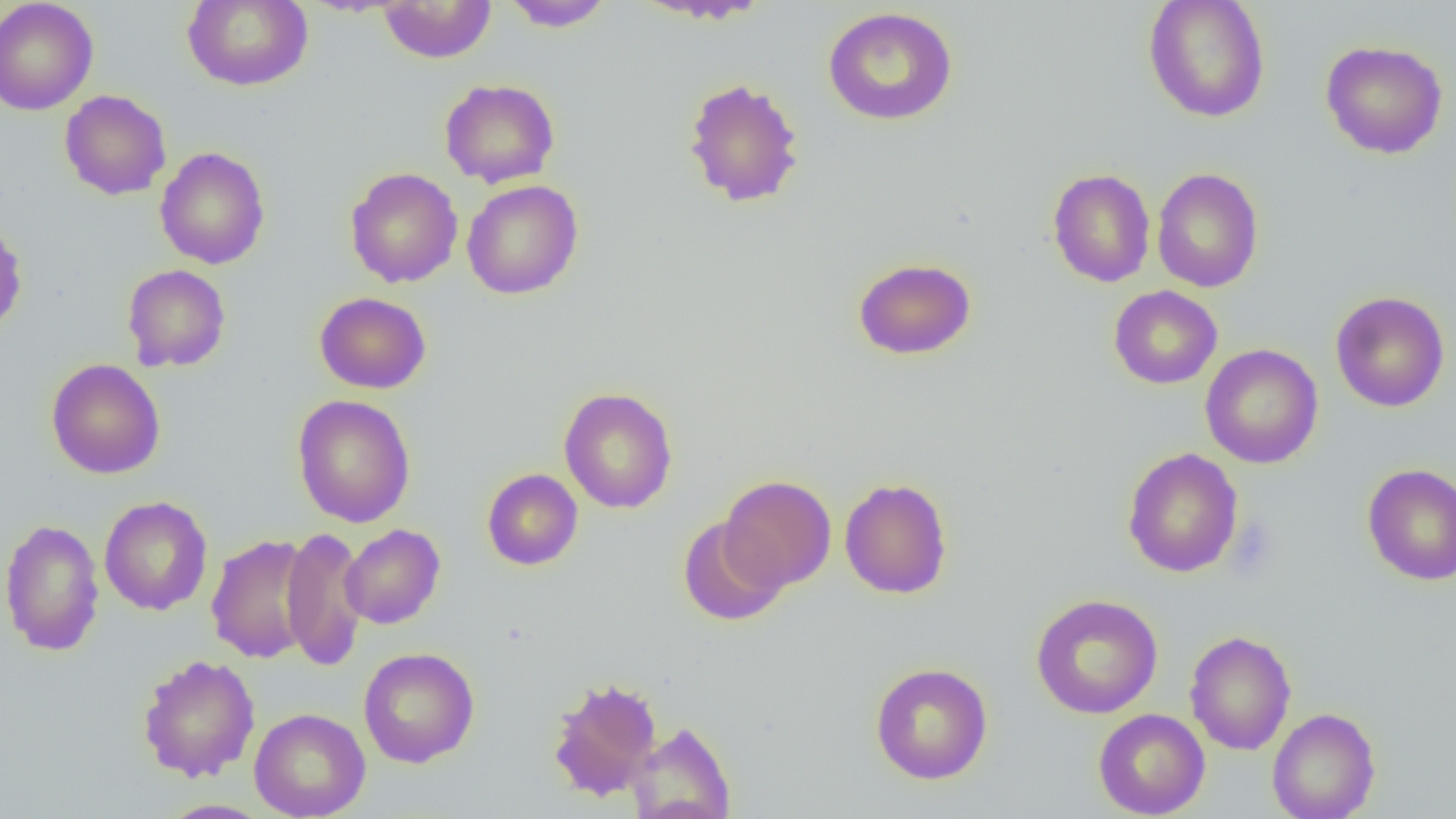 Approximate bounding boxes as named x1/y1/x2/y2 corners in pixels. Uninfected red blood cell locations: (x1=0, y1=0, x2=99, y2=116), (x1=182, y1=0, x2=313, y2=91), (x1=502, y1=0, x2=615, y2=32), (x1=631, y1=0, x2=773, y2=25), (x1=1143, y1=0, x2=1271, y2=123), (x1=377, y1=1, x2=496, y2=63), (x1=822, y1=6, x2=958, y2=126), (x1=1320, y1=40, x2=1448, y2=159), (x1=682, y1=76, x2=805, y2=208), (x1=439, y1=78, x2=560, y2=188), (x1=59, y1=90, x2=172, y2=200), (x1=154, y1=146, x2=270, y2=270), (x1=344, y1=167, x2=463, y2=288), (x1=1151, y1=167, x2=1264, y2=293), (x1=1047, y1=168, x2=1156, y2=287), (x1=462, y1=179, x2=584, y2=300), (x1=0, y1=218, x2=27, y2=337), (x1=852, y1=257, x2=977, y2=360), (x1=121, y1=264, x2=231, y2=372), (x1=1108, y1=285, x2=1223, y2=389), (x1=314, y1=291, x2=431, y2=394), (x1=1331, y1=291, x2=1450, y2=413), (x1=1200, y1=344, x2=1324, y2=469), (x1=46, y1=359, x2=165, y2=479), (x1=558, y1=387, x2=678, y2=513), (x1=292, y1=394, x2=416, y2=528), (x1=1122, y1=447, x2=1243, y2=578), (x1=1362, y1=463, x2=1456, y2=586), (x1=482, y1=468, x2=583, y2=570), (x1=720, y1=475, x2=836, y2=591), (x1=839, y1=477, x2=952, y2=599), (x1=98, y1=496, x2=213, y2=616), (x1=677, y1=517, x2=789, y2=626), (x1=1, y1=518, x2=104, y2=656), (x1=340, y1=524, x2=445, y2=629), (x1=280, y1=526, x2=368, y2=671), (x1=206, y1=534, x2=317, y2=664), (x1=1030, y1=593, x2=1164, y2=719), (x1=1184, y1=629, x2=1297, y2=756), (x1=358, y1=646, x2=480, y2=768), (x1=137, y1=653, x2=260, y2=782), (x1=870, y1=662, x2=993, y2=784), (x1=547, y1=676, x2=662, y2=802), (x1=249, y1=707, x2=371, y2=819), (x1=1267, y1=707, x2=1381, y2=819), (x1=1093, y1=708, x2=1210, y2=818), (x1=627, y1=721, x2=737, y2=819), (x1=159, y1=799, x2=270, y2=818). Slide-level diagnosis: no evidence of blood parasites. Light microscopy. Thin blood smear. One field of a larger specimen. Image is 1456×819 pixels. 1000x magnification.